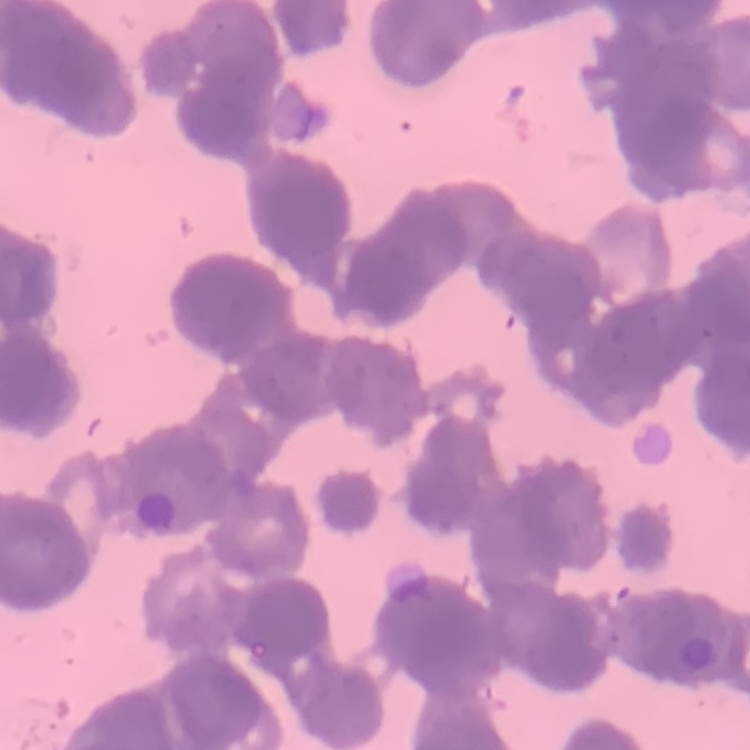 The erythrocytes exhibit rouleaux formation. Field's or Giemsa stain. Square crop of a larger photomicrograph. Thin blood film.